Point out every Plasmodium parasite.
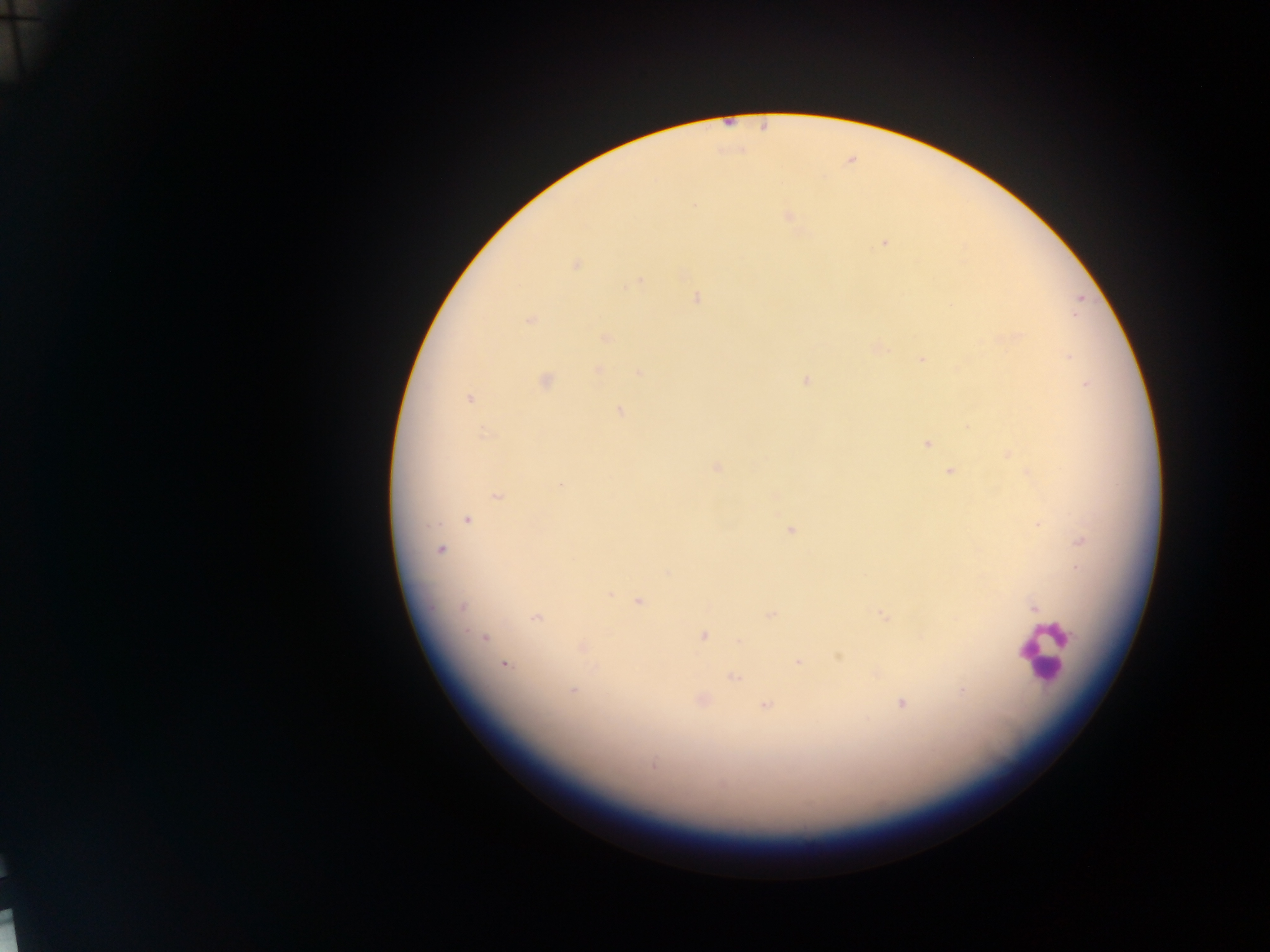
Approximate centers as [x, y] in pixels.
Plasmodium parasites: [694, 206], [788, 215], [885, 243], [576, 265], [638, 281], [697, 298], [530, 319], [605, 337], [1018, 337], [1068, 357], [922, 359], [599, 370], [639, 373], [544, 381], [805, 381], [1087, 384], [469, 399], [620, 412], [484, 434], [927, 444], [1009, 454], [716, 468], [950, 470], [560, 484], [497, 496], [467, 519], [1037, 524], [790, 530], [1081, 540], [441, 549], [668, 573], [610, 594], [639, 602], [462, 607], [1034, 608], [771, 615], [883, 615], [535, 618], [465, 632], [703, 636], [485, 638], [739, 642], [582, 647], [839, 657], [797, 662], [504, 665], [597, 668], [878, 674], [734, 677], [573, 690], [962, 690], [701, 700], [901, 703], [765, 706], [653, 764], [723, 785].

image size = 1270×952 pixels
capture = mobile-phone photograph through a microscope
preparation = thick blood smear
country = Ghana
leukocyte locations = approximate centers as [x, y] in pixels: [1045, 651]
field of view = single